Identify the parasite.
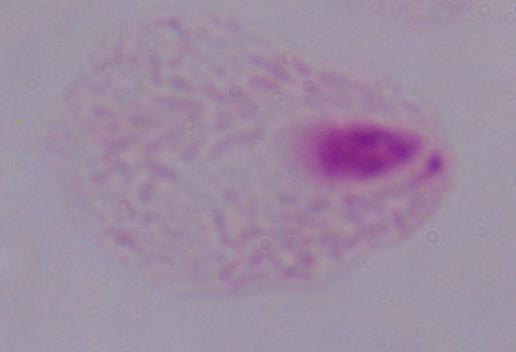

A trichomonad.

Summary:
  - Modality: photomicrograph
  - Magnification: 1000x